Comment on the morphology of the red blood cells.
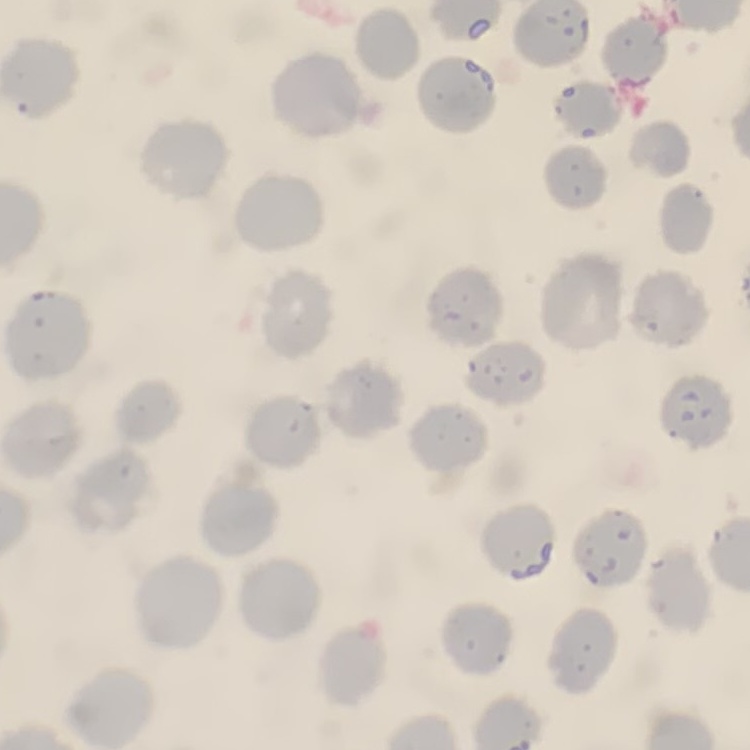
No rouleaux formation.

Summary:
  - Image type: one tile cut from a larger photomicrograph
  - Stain: Field's or Giemsa
  - Preparation: thin peripheral smear